Outline each blood parasite and name the species.
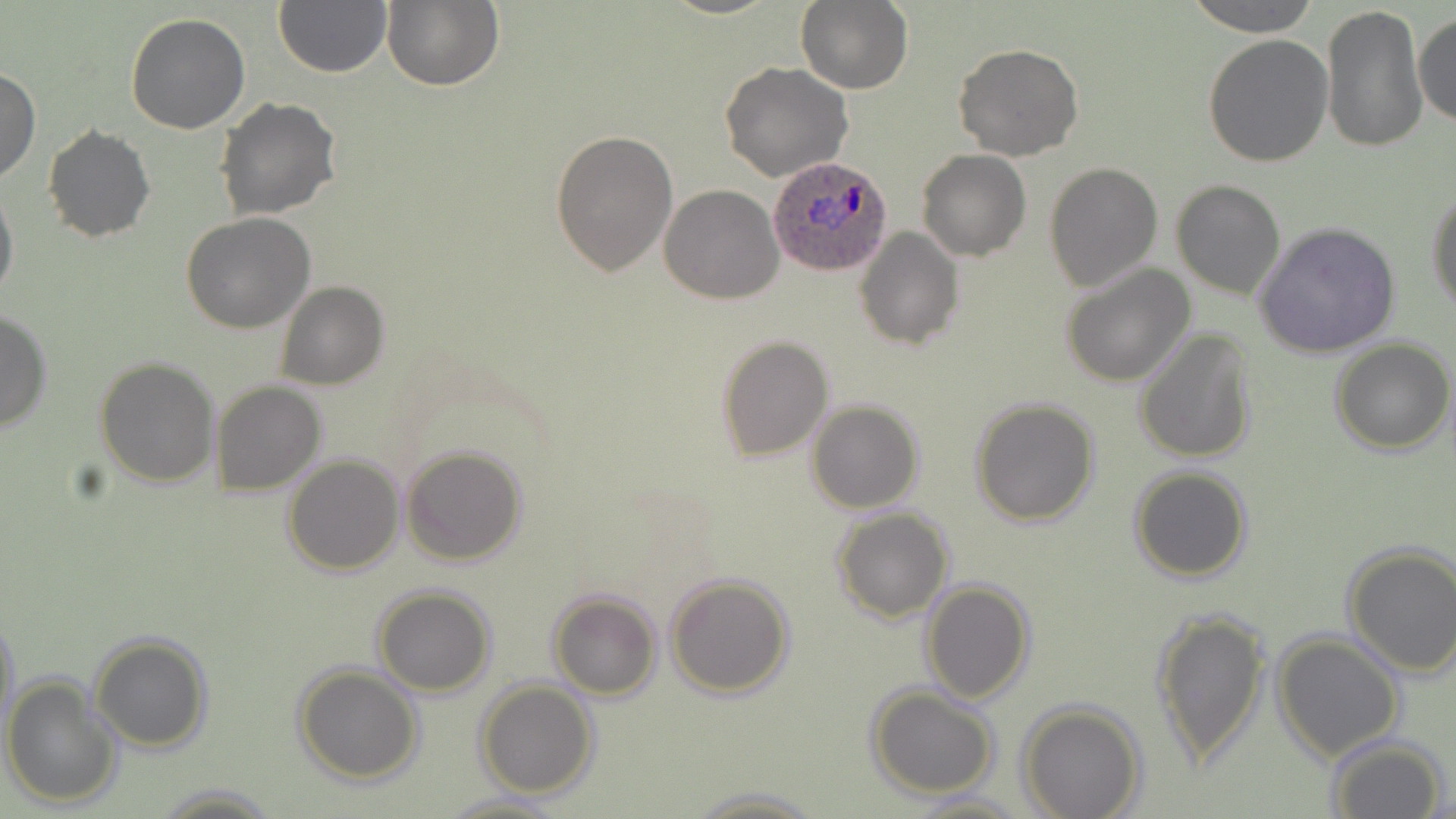

Approximate bounding boxes as (x1,y1)-(x2,y2) corner pairs in pixels.
Plasmodium ovale-infected red blood cells: (768,154)-(894,279).
No Plasmodium falciparum, Plasmodium malariae, Plasmodium vivax, Babesia divergens, or Trypanosoma brucei observed.

Uninfected red blood cell locations: (797,0)-(912,93), (1186,0)-(1321,37), (274,1)-(391,77), (381,1)-(503,91), (1320,2)-(1426,153), (1414,10)-(1455,128), (125,12)-(251,134), (1203,33)-(1334,169), (953,43)-(1083,161), (721,61)-(853,183), (0,65)-(39,185), (215,96)-(342,223), (43,124)-(156,244), (549,127)-(677,277), (918,148)-(1031,261), (1044,160)-(1163,292), (0,179)-(18,308), (1172,180)-(1286,299), (660,183)-(784,303), (1426,190)-(1456,314), (181,213)-(317,333), (1256,222)-(1401,360), (855,226)-(963,349), (1061,262)-(1195,387), (276,280)-(390,390), (0,307)-(54,434), (1135,327)-(1256,464), (716,335)-(833,460), (1331,339)-(1454,454), (94,358)-(220,486), (210,381)-(325,495), (970,396)-(1100,526), (807,400)-(923,513), (401,445)-(529,566), (281,454)-(405,575), (1131,466)-(1252,582), (832,509)-(954,623), (1341,541)-(1456,677), (665,572)-(795,699), (921,580)-(1034,702), (371,586)-(495,696), (548,591)-(661,700), (1,608)-(19,742), (1151,608)-(1268,772), (1272,631)-(1404,762), (89,634)-(213,751), (294,664)-(423,784), (3,676)-(120,809), (477,679)-(598,799), (864,686)-(999,798), (1017,700)-(1146,819), (1328,736)-(1450,819), (150,782)-(282,818), (684,785)-(825,817), (439,791)-(567,818), (904,791)-(1025,818). Slide-level diagnosis: Plasmodium ovale. Light microscopy. One field of a larger specimen. May-Grünwald-Giemsa-stained preparation. Image is 1456×819 pixels. Captured at 1000x magnification. Thin blood smear.